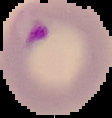

Summary:
  - Image type: cell region segmented out of the field of view; surrounding area masked to black
  - Image size: 112×118 pixels
  - Preparation: thin blood film
  - Malaria status: parasitized